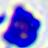
Summary:
  - Magnification: 400x
  - Modality: photomicrograph
  - Identification: white blood cell